Give the preparation type.
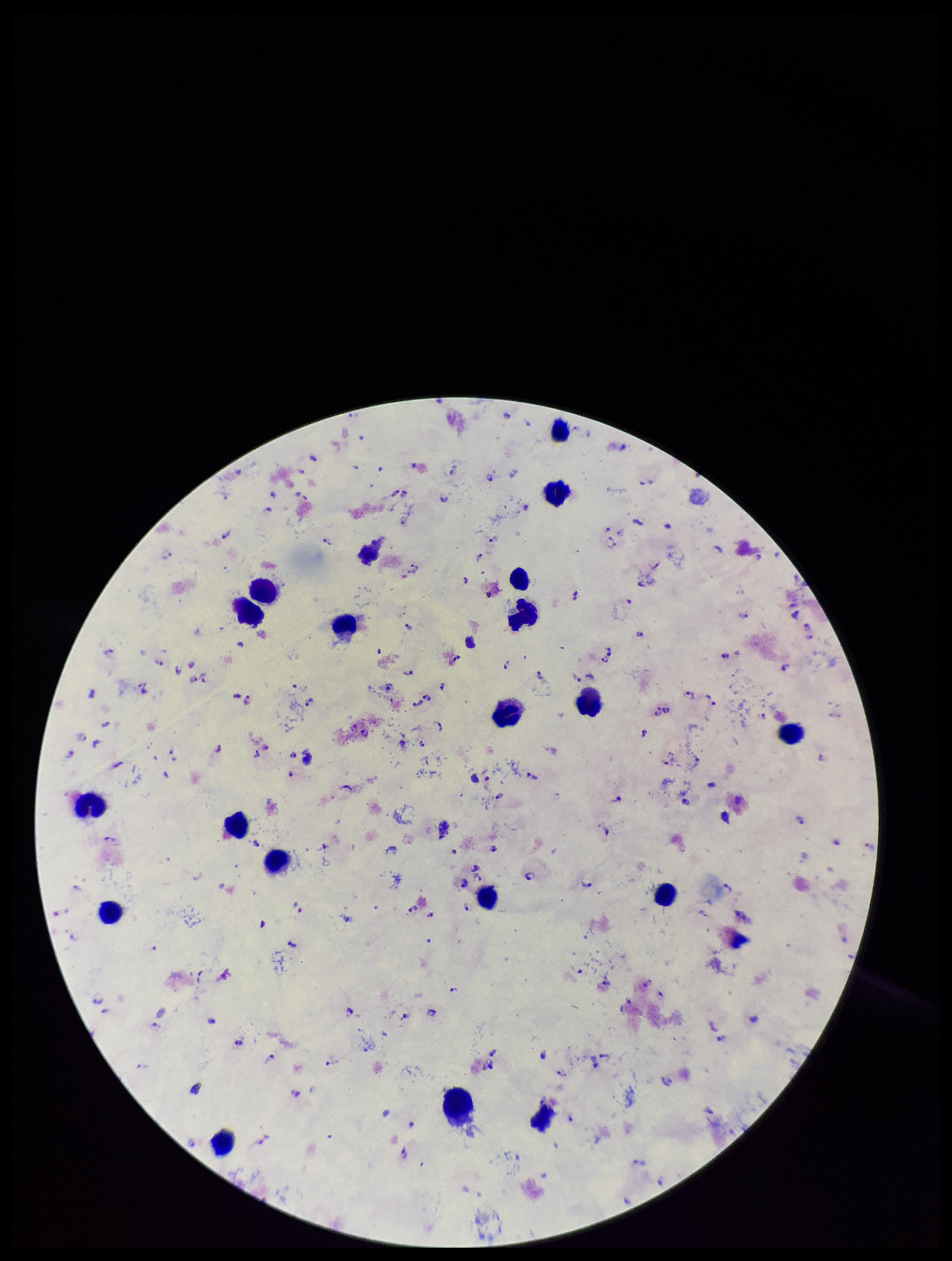
It is a thick blood smear.

Image is 952×1261 pixels. Photographed through the microscope eyepiece with a smartphone camera. Single field of view. Patient malaria status: infected. Stained with Giemsa. Parasite count: 112. Leukocyte count: 20. Plasmodium parasites: seen. Species reported for this patient: Plasmodium falciparum.